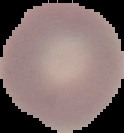
malaria status = uninfected
image size = 124×133 pixels
preparation = thin blood film
image type = segmented cell region on a black background